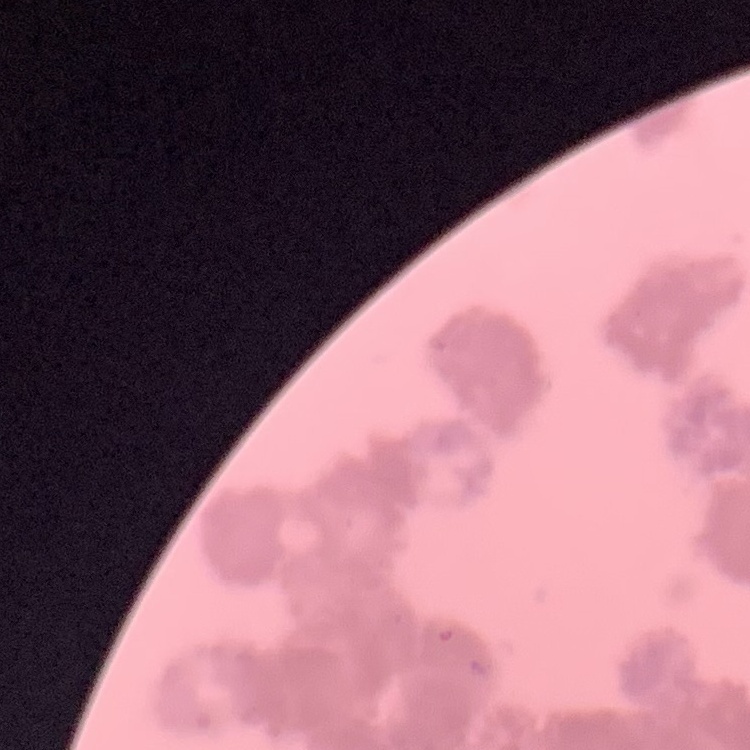
Summary:
  - Erythrocyte morphology: rouleaux formation
  - Preparation: thin blood film
  - Stain: Field's or Giemsa
  - Image type: one tile cut from a larger photomicrograph